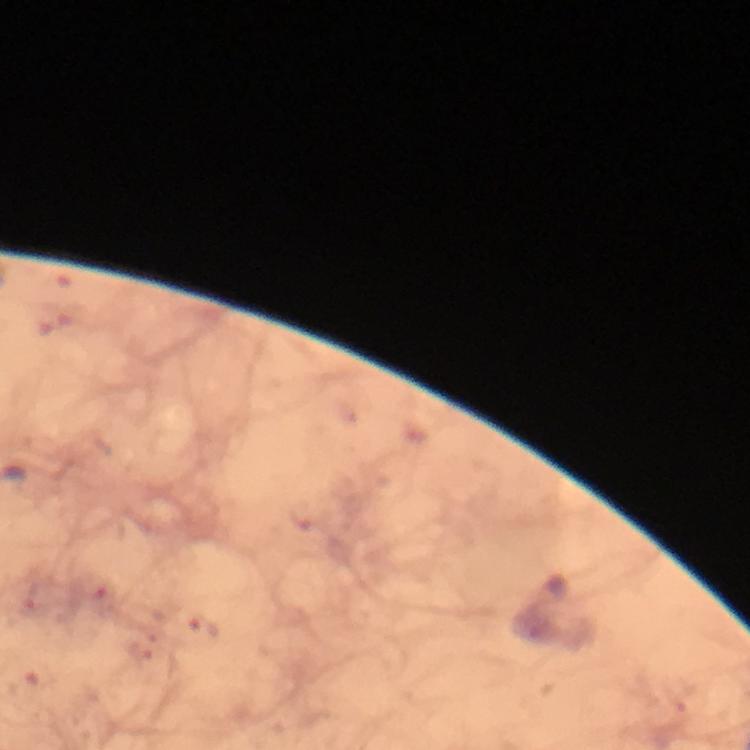
Approximate object centers, in pixels from the top-left corner. Malaria parasite locations: (x=203, y=628). Photographed through the microscope with a smartphone camera. Image is 750×750 pixels. From a malaria diagnostic workup. Thick blood smear. Giemsa-stained preparation. At 100x magnification. A crop from one field of view. Immersion oil was used.